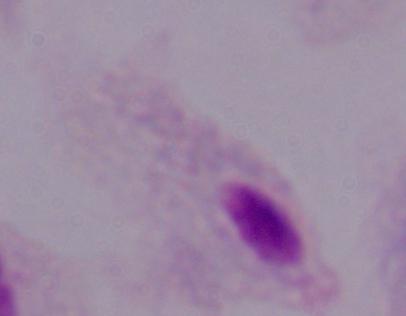

{
  "modality": "micrograph",
  "magnification": "1000x",
  "identification": "trichomonad"
}